Outline each Plasmodium vivax-infected red blood cell.
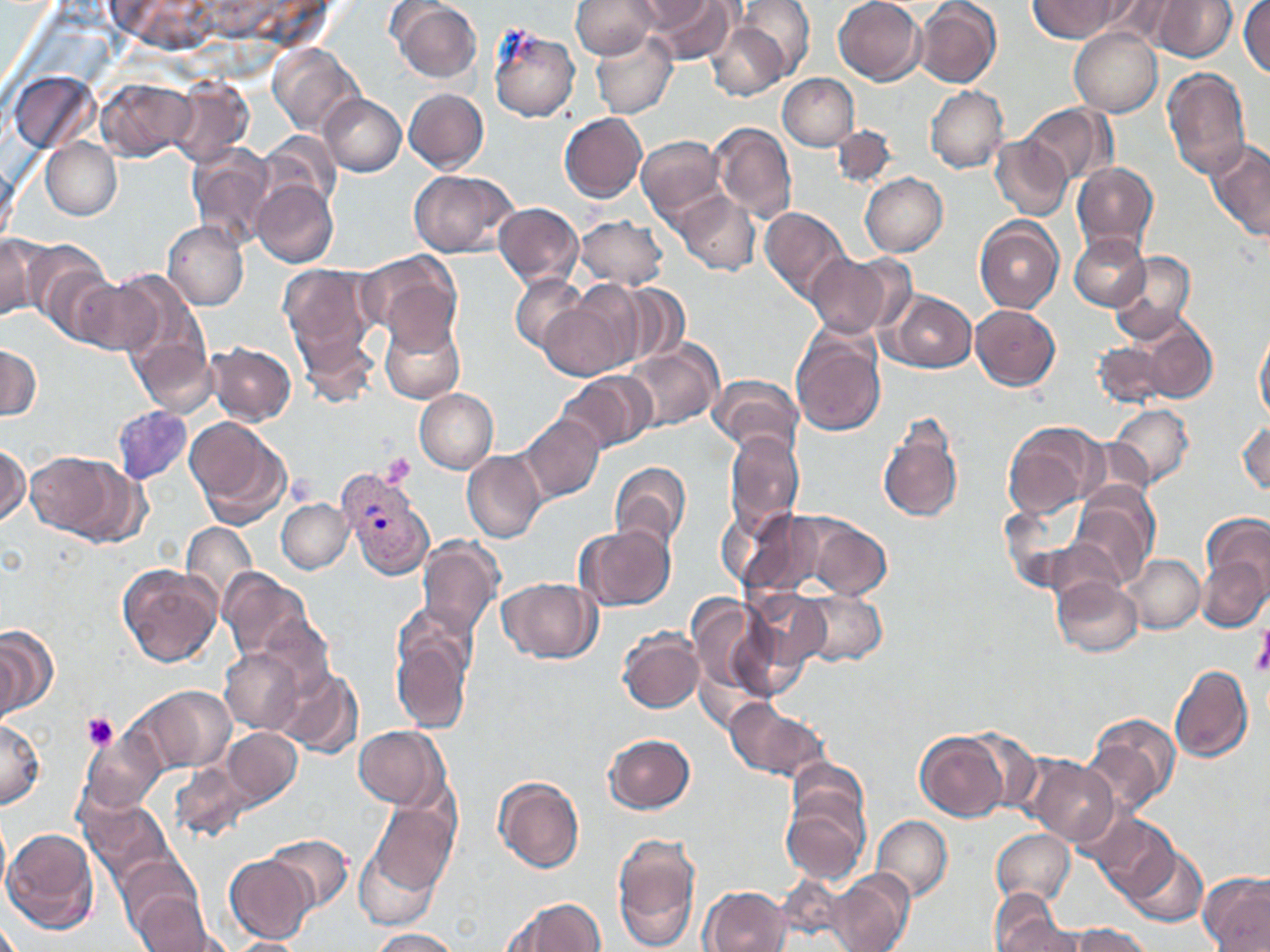
Approximate bounding boxes as (x1, y1, x2, y2) in pixels.
Plasmodium vivax-infected red blood cells: (337, 465, 435, 581).

Summary:
  - Uninfected red blood cell locations: (572, 0, 662, 58), (629, 0, 718, 32), (638, 0, 737, 63), (835, 0, 926, 84), (915, 0, 1002, 88), (1029, 0, 1125, 42), (1096, 0, 1181, 47), (1150, 0, 1236, 62), (736, 1, 815, 79), (1239, 1, 1270, 77), (389, 2, 482, 81), (706, 18, 793, 102), (487, 24, 580, 122), (1070, 29, 1163, 116), (589, 30, 676, 118), (268, 45, 364, 136), (1161, 67, 1252, 181), (11, 69, 98, 154), (778, 73, 859, 150), (97, 76, 193, 159), (169, 77, 253, 168), (926, 86, 1007, 173), (404, 88, 489, 174), (320, 93, 405, 176), (1021, 102, 1112, 189), (558, 112, 650, 202), (712, 121, 797, 221), (832, 123, 901, 188), (636, 134, 725, 220), (990, 135, 1072, 221), (1205, 135, 1270, 244), (41, 137, 122, 220), (187, 151, 274, 253), (1072, 160, 1160, 251), (408, 168, 516, 257), (860, 172, 948, 256), (253, 181, 338, 269), (672, 190, 760, 275), (492, 202, 582, 289), (759, 206, 852, 303), (574, 216, 670, 290), (975, 218, 1065, 311), (162, 221, 249, 311), (1070, 233, 1149, 310), (0, 234, 46, 323), (28, 243, 115, 339), (356, 250, 464, 349), (803, 250, 909, 339), (1106, 250, 1197, 342), (279, 263, 381, 381), (96, 273, 199, 372), (510, 276, 587, 352), (72, 279, 162, 357), (617, 284, 690, 367), (541, 287, 641, 379), (885, 290, 977, 372), (970, 304, 1061, 390), (126, 305, 217, 417), (379, 315, 465, 404), (1136, 319, 1217, 405), (1254, 321, 1270, 424), (791, 326, 887, 438), (1092, 339, 1171, 410), (623, 340, 724, 433), (206, 342, 297, 425), (0, 344, 40, 422), (555, 374, 651, 455), (710, 374, 803, 457), (414, 389, 498, 473), (1108, 403, 1194, 489), (112, 405, 193, 484), (876, 411, 965, 527), (519, 414, 605, 504), (185, 416, 292, 526), (1236, 417, 1269, 496), (1002, 420, 1106, 520), (724, 431, 803, 538), (0, 440, 28, 529), (25, 449, 138, 543), (462, 450, 546, 542), (610, 461, 691, 555), (1073, 484, 1158, 584), (276, 498, 354, 574), (758, 507, 897, 604), (1202, 510, 1270, 607), (181, 521, 257, 607), (577, 524, 677, 612), (418, 536, 502, 639), (1125, 552, 1204, 633), (1198, 556, 1267, 631), (116, 563, 221, 667), (216, 568, 316, 666), (1051, 576, 1142, 658), (499, 577, 599, 664), (743, 588, 832, 677), (799, 589, 887, 667), (687, 592, 772, 705), (390, 621, 473, 734), (0, 624, 57, 719), (618, 628, 704, 713), (219, 645, 306, 734), (1169, 663, 1253, 763), (274, 665, 362, 758), (129, 685, 237, 776), (725, 698, 827, 781), (1085, 712, 1181, 820), (0, 716, 45, 811), (222, 726, 302, 807), (354, 726, 445, 809), (915, 730, 1009, 820), (602, 733, 694, 813), (81, 734, 165, 817), (1024, 755, 1119, 846), (167, 760, 254, 846), (492, 776, 586, 874), (781, 790, 872, 888), (80, 791, 176, 890), (360, 797, 461, 919), (1087, 812, 1182, 901), (0, 813, 12, 911), (871, 814, 953, 903), (3, 826, 99, 935), (992, 829, 1075, 905), (261, 832, 353, 914), (610, 832, 702, 949), (1126, 842, 1207, 927), (224, 854, 316, 944), (825, 871, 913, 952), (1200, 872, 1270, 952), (121, 877, 214, 952), (700, 886, 791, 952), (989, 891, 1075, 952), (498, 897, 608, 952), (1067, 925, 1157, 952), (365, 927, 464, 951), (223, 938, 312, 952)
  - Platelet locations: (381, 454, 416, 487), (1253, 626, 1270, 678), (82, 712, 119, 753)
  - Slide-level diagnosis: Plasmodium vivax
  - Magnification: 1000x
  - Preparation: thin blood film
  - Field of view: one of a larger specimen
  - Image size: 1270×952 pixels
  - Stain: May-Grünwald-Giemsa
  - Modality: light microscopy